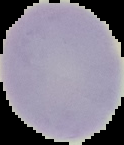

Image is 124×145 pixels. Result: no Plasmodium parasites seen. From a thin blood smear. The area outside the segmented cell region is set to black.